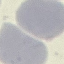
Summary:
  - Result: no malaria parasites detected
  - Preparation: thin blood smear
  - Stain: Giemsa
  - Image type: automatically extracted cell patch, resized to 64 × 64 pixels
  - Capture: smartphone camera at the microscope eyepiece